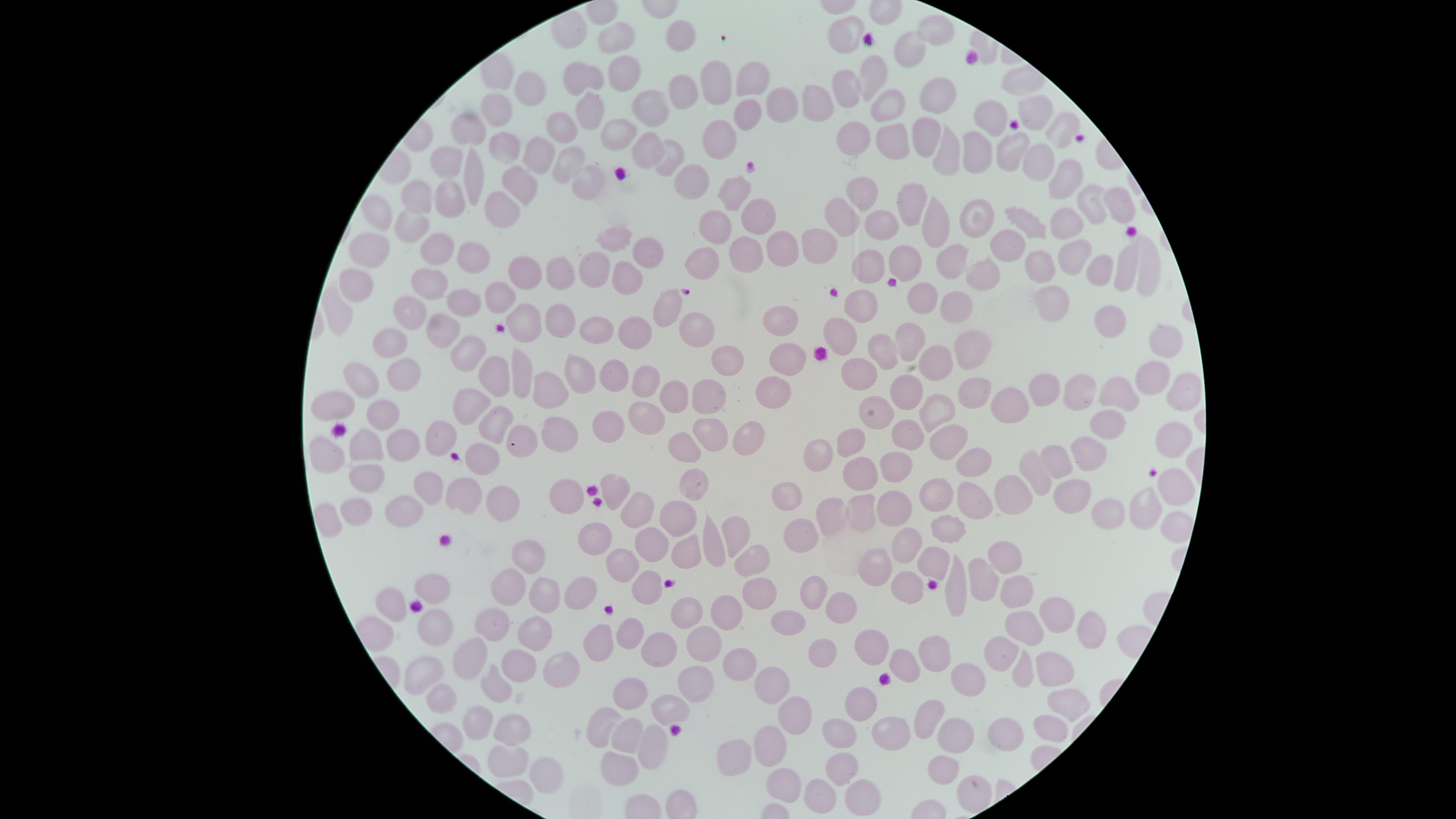

Approximate marker points as {x, y} in pixels.
Summary:
  - Uninfected red blood cells: {936, 26}, {843, 29}, {679, 36}, {622, 37}, {904, 51}, {623, 68}, {875, 68}, {586, 75}, {758, 76}, {720, 78}, {525, 86}, {676, 86}, {848, 91}, {931, 98}, {883, 100}, {647, 103}, {502, 106}, {821, 107}, {593, 108}, {781, 109}, {1039, 110}, {753, 113}, {997, 117}, {465, 124}, {564, 128}, {1059, 129}, {922, 131}, {622, 132}, {856, 132}, {727, 135}, {893, 138}, {510, 141}, {644, 144}, {539, 145}, {674, 148}, {1015, 149}, {975, 150}, {944, 156}, {566, 158}, {1032, 160}, {451, 161}, {1066, 178}, {694, 179}, {468, 180}, {587, 180}, {522, 186}, {743, 188}, {856, 190}, {448, 196}, {419, 199}, {1114, 201}, {914, 202}, {1089, 203}, {503, 208}, {983, 208}, {753, 209}, {380, 212}, {830, 215}, {938, 216}, {1029, 217}, {720, 221}, {894, 222}, {1064, 222}, {411, 223}, {1003, 236}, {613, 240}, {375, 241}, {785, 242}, {817, 243}, {441, 247}, {748, 247}, {653, 249}, {1078, 250}, {477, 252}, {907, 254}, {951, 261}, {1124, 263}, {1146, 263}, {703, 264}, {875, 264}, {1040, 266}, {557, 267}, {600, 267}, {528, 268}, {1095, 271}, {977, 274}, {628, 277}, {358, 278}, {428, 285}, {929, 293}, {497, 295}, {1049, 298}, {463, 302}, {670, 302}, {961, 303}, {342, 309}, {863, 309}, {407, 310}, {524, 317}, {1107, 317}, {551, 318}, {783, 323}, {692, 326}, {600, 327}, {443, 328}, {627, 328}, {839, 333}, {913, 335}, {392, 340}, {1171, 341}, {975, 346}, {883, 347}, {464, 351}, {722, 355}, {935, 360}, {791, 361}, {615, 367}, {403, 368}, {491, 373}, {1151, 373}, {576, 376}, {862, 376}, {363, 378}, {521, 378}, {645, 378}, {776, 387}, {1181, 387}, {912, 389}, {549, 391}, {715, 391}, {970, 393}, {1045, 393}, {1084, 393}, {1115, 393}, {683, 396}, {338, 401}, {472, 402}, {1009, 402}, {936, 407}, {384, 410}, {876, 413}, {641, 415}, {608, 416}, {498, 417}, {1108, 422}, {563, 425}, {701, 427}, {905, 427}, {948, 437}, {519, 439}, {440, 440}, {738, 440}, {851, 441}, {1169, 441}, {681, 446}, {361, 447}, {401, 453}, {975, 454}, {825, 455}, {1057, 455}, {1086, 455}, {480, 457}, {325, 458}, {898, 465}, {1040, 465}, {863, 471}, {364, 480}, {692, 482}, {1171, 482}, {621, 484}, {427, 485}, {791, 491}, {967, 491}, {465, 493}, {937, 493}, {1076, 493}, {1018, 495}, {567, 499}, {508, 504}, {1143, 507}, {356, 508}, {859, 508}, {894, 508}, {399, 510}, {638, 510}, {1115, 511}, {831, 515}, {679, 516}, {945, 520}, {737, 525}, {600, 531}, {808, 536}, {909, 540}, {715, 543}, {649, 546}, {687, 547}, {533, 552}, {1003, 557}, {754, 558}, {630, 559}, {878, 562}, {932, 562}, {982, 579}, {903, 584}, {430, 585}, {575, 585}, {818, 585}, {649, 586}, {763, 587}, {508, 589}, {1014, 589}, {547, 591}, {957, 593}, {394, 603}, {1051, 610}, {727, 611}, {844, 612}, {690, 614}, {789, 617}, {493, 623}, {433, 625}, {1083, 626}, {634, 629}, {1031, 631}, {540, 633}, {708, 635}, {866, 640}, {600, 646}, {822, 649}, {1000, 652}, {664, 653}, {931, 654}, {470, 660}, {522, 660}, {738, 660}, {902, 662}, {563, 669}, {1022, 670}, {419, 673}, {1051, 673}, {501, 679}, {699, 681}, {971, 681}, {770, 682}, {638, 690}, {441, 699}, {866, 702}, {1066, 703}, {672, 705}, {798, 710}, {934, 719}, {469, 723}, {602, 723}, {1048, 727}, {893, 731}, {959, 732}, {847, 733}, {510, 734}, {1008, 734}, {627, 735}, {654, 739}, {775, 742}, {738, 753}, {510, 757}, {615, 761}, {944, 764}, {837, 768}, {543, 771}, {783, 781}, {971, 784}, {819, 793}, {860, 797}
  - Preparation: thin smear of blood
  - Stain: Giemsa
  - Presence: no malaria parasites identified
  - Visible region: circular
  - Capture: smartphone photograph through the microscope eyepiece
  - Image size: 1456×819 pixels
  - Field of view: single